Identify the blood parasite species.
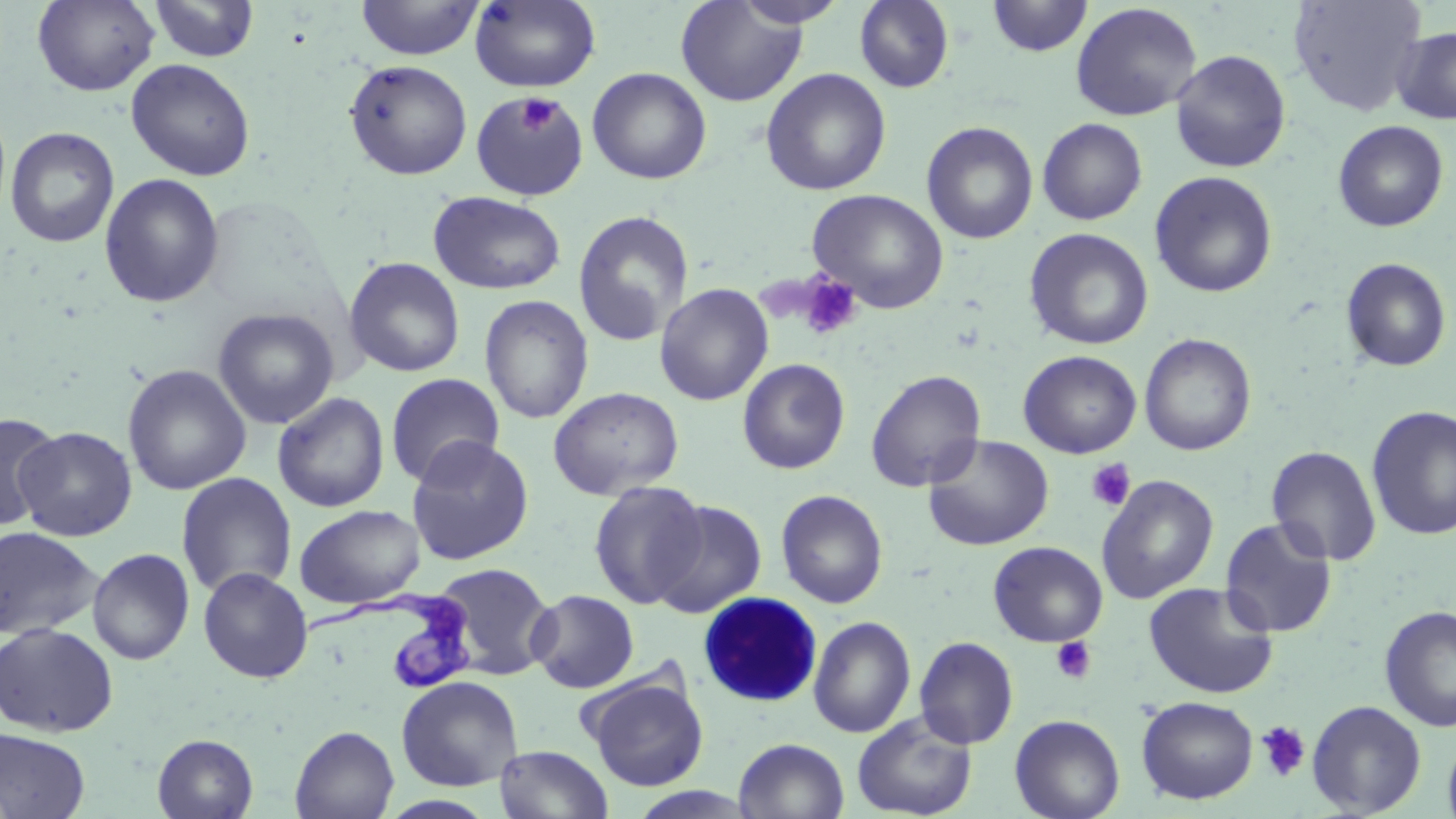
Trypanosoma brucei.

Summary:
  - Coordinate format: approximate bounding boxes as (x1,y1)-(x2,y2) corner pairs in pixels
  - White blood cell locations: (697,592)-(823,706)
  - Uninfected red blood cell locations: (32,0)-(160,95), (149,0)-(259,62), (355,0)-(485,61), (470,0)-(601,92), (733,0)-(848,29), (986,0)-(1092,57), (1288,0)-(1427,116), (675,1)-(808,107), (854,1)-(954,93), (1070,3)-(1202,121), (1392,26)-(1456,125), (1169,50)-(1291,173), (126,58)-(256,181), (344,59)-(472,180), (587,67)-(712,184), (760,68)-(891,196), (470,90)-(590,201), (1037,118)-(1148,225), (1332,120)-(1449,232), (921,121)-(1038,244), (4,126)-(120,248), (1149,171)-(1278,298), (99,173)-(225,308), (807,188)-(950,313), (428,191)-(566,295), (572,210)-(695,347), (1024,228)-(1154,350), (344,256)-(465,377), (1340,258)-(1452,372), (654,283)-(774,406), (479,295)-(594,424), (212,307)-(339,429), (1139,333)-(1257,456), (1018,350)-(1141,458), (737,358)-(850,474), (122,363)-(252,495), (865,369)-(987,492), (385,373)-(505,488), (549,386)-(684,500), (272,392)-(390,513), (1366,405)-(1456,541), (0,411)-(62,530), (15,426)-(137,541), (922,434)-(1055,551), (406,436)-(534,566), (1265,445)-(1382,566), (175,472)-(297,598), (1096,474)-(1219,603), (588,481)-(708,609), (775,489)-(888,608), (650,500)-(767,618), (294,504)-(426,609), (1219,516)-(1338,638), (0,526)-(103,640), (988,541)-(1108,647), (88,548)-(195,665), (430,562)-(557,680), (198,566)-(313,683), (1144,581)-(1279,699), (528,589)-(639,693), (1379,605)-(1456,732), (808,615)-(916,738), (0,622)-(119,737), (914,636)-(1018,750), (396,675)-(523,791), (586,676)-(708,791), (1136,696)-(1258,804), (1307,700)-(1427,817), (852,710)-(977,819), (1009,710)-(1261,812), (1010,714)-(1125,819), (290,725)-(400,819), (0,727)-(91,818), (1443,732)-(1456,819), (152,733)-(258,818), (734,738)-(849,819), (494,744)-(613,818), (377,794)-(498,818)
  - Trypanosoma brucei locations: (303,588)-(475,690)
  - Platelet locations: (517,95)-(560,134), (797,273)-(863,340), (1085,457)-(1136,512), (1050,637)-(1097,683), (1256,721)-(1311,782)
  - Magnification: 1000x
  - Preparation: thin blood film
  - Field of view: one of a larger specimen
  - Stain: May-Grünwald-Giemsa
  - Modality: light microscopy
  - Image size: 1456×819 pixels